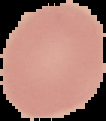 Malaria status: uninfected. Image is 106×121 pixels. From a thin blood smear. Segmented cell region on a black background.